Give a bounding box for every Plasmodium parasite.
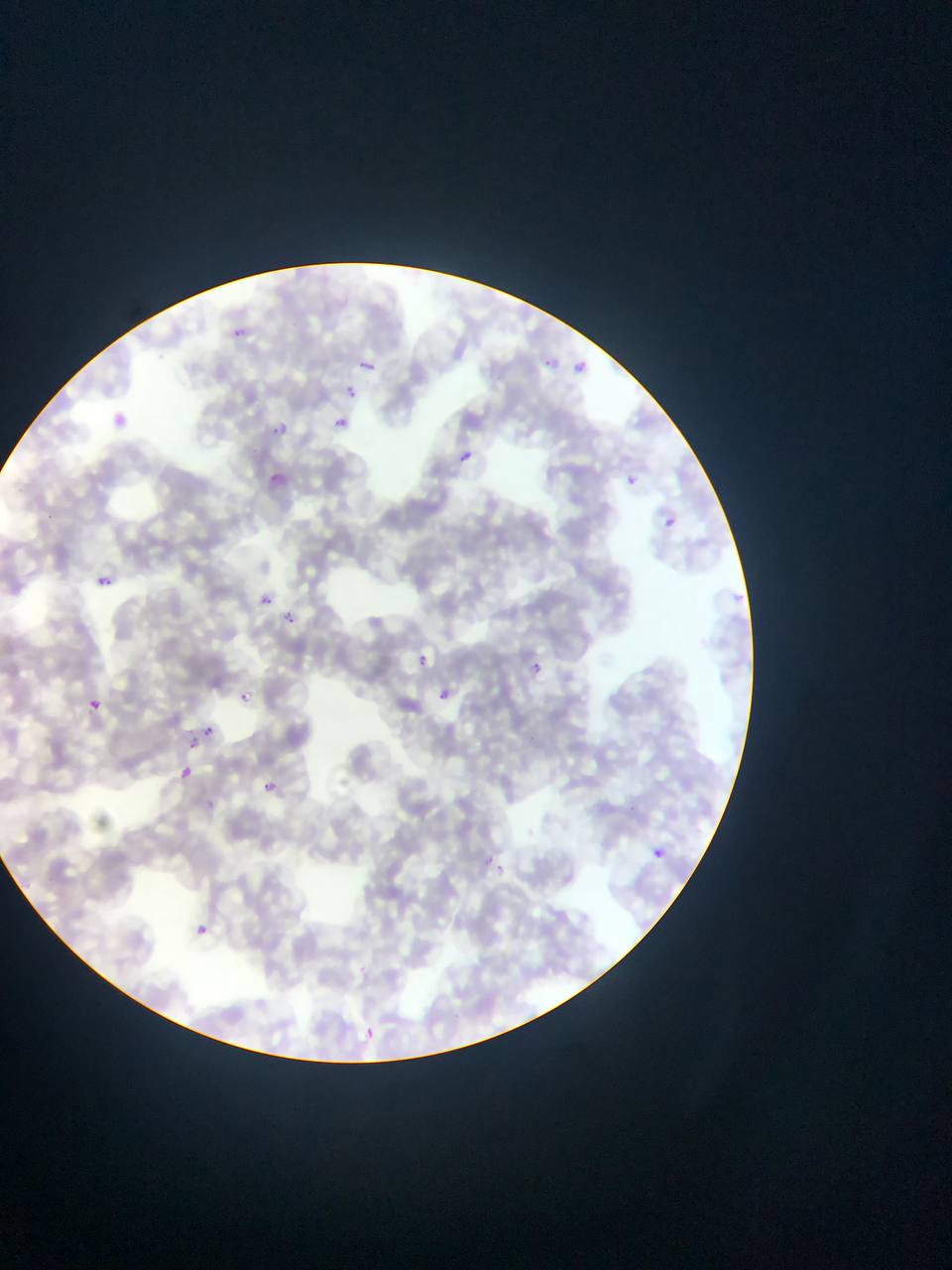

Approximate bounding boxes as {left, top, right, bottom} in pixels.
Plasmodium parasites: {230, 322, 267, 342}, {539, 349, 556, 369}, {359, 353, 381, 371}, {569, 357, 590, 375}, {345, 382, 360, 399}, {100, 402, 128, 421}, {270, 408, 293, 432}, {334, 409, 353, 427}, {462, 450, 475, 463}, {265, 467, 295, 496}, {625, 472, 638, 492}, {662, 515, 676, 537}, {92, 569, 116, 592}, {726, 587, 746, 599}, {262, 592, 276, 609}, {275, 606, 302, 640}, {413, 650, 431, 664}, {531, 659, 543, 674}, {429, 682, 456, 704}, {85, 692, 104, 710}, {240, 692, 251, 704}, {203, 725, 216, 737}, {189, 738, 199, 750}, {179, 765, 194, 780}, {262, 773, 285, 796}, {476, 849, 497, 870}, {654, 849, 664, 857}, {193, 917, 213, 940}, {356, 1019, 380, 1044}.

Summary:
  - Image size: 952×1270 pixels
  - Country: Ghana
  - Field of view: single
  - Preparation: thin blood film
  - Capture: mobile-phone photograph through a microscope